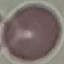

Summary:
  - Result: no malaria parasites detected
  - Image type: cell patch, automatically extracted from a larger field of view and resized to 64 × 64 pixels
  - Preparation: thin blood smear
  - Capture: smartphone through the microscope eyepiece
  - Stain: Giemsa